Classify this cell by malaria status.
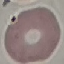

Uninfected.

preparation = thin blood film
image type = cell patch, automatically extracted from a larger field of view and resized to 64 × 64 pixels
capture = smartphone camera at the microscope eyepiece
stain = Giemsa